Assess this cell for malaria.
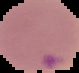
Parasitized.

From a thin blood smear. Cell region segmented out of the field of view; the surrounding area is masked to black. Image is 79×73 pixels.